State the blood parasite species.
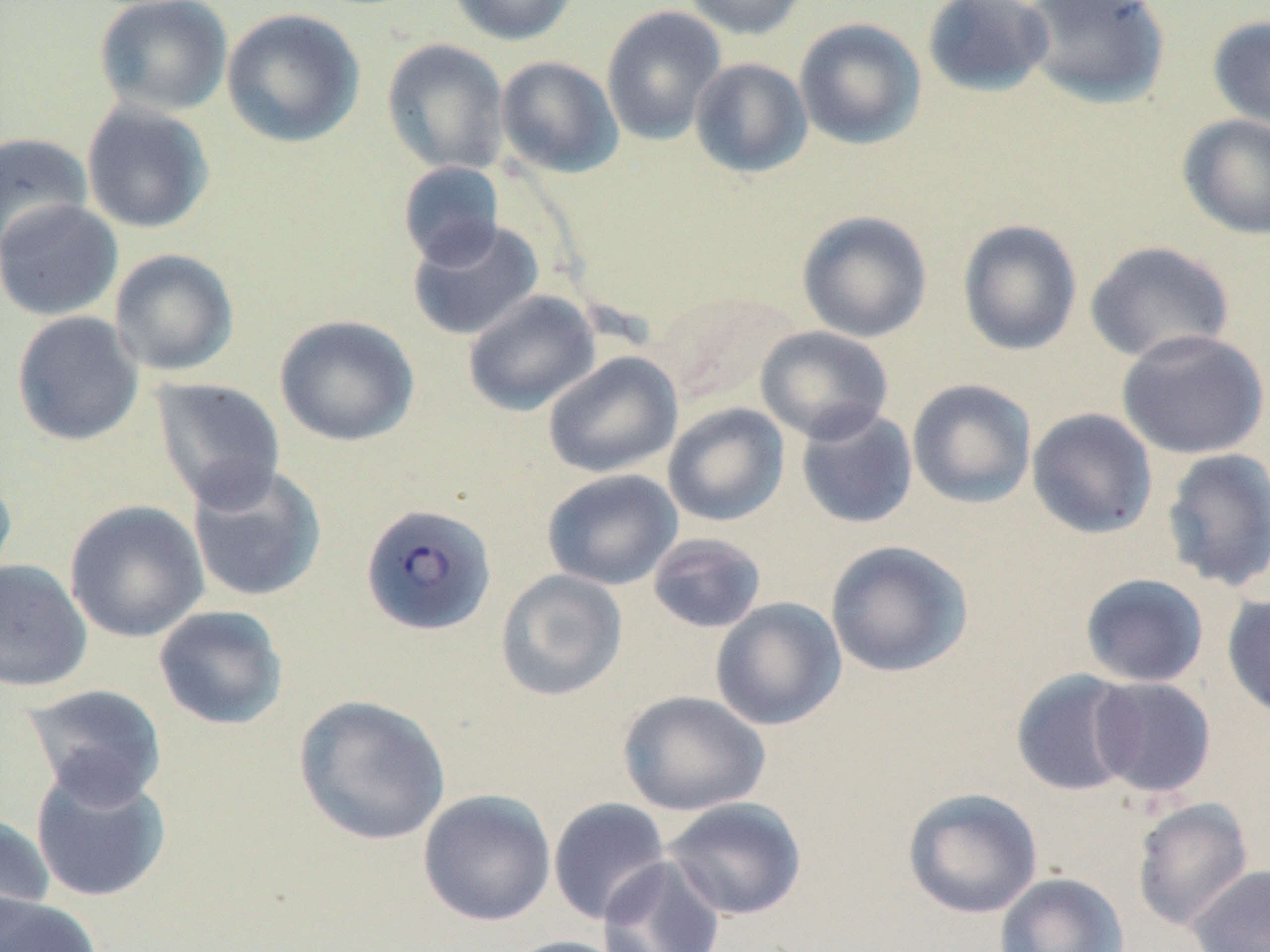
Plasmodium falciparum.

preparation = thin blood smear
magnification = 1000x
field of view = single
modality = optical microscopy
stain = May-Grünwald-Giemsa
Plasmodium falciparum-infected red blood cell locations = approximate bounding boxes as [x1, y1, x2, y2] in pixels: [359, 503, 497, 636]
image size = 1270×952 pixels
uninfected red blood cell locations = approximate bounding boxes as [x1, y1, x2, y2] in pixels: [447, 0, 579, 46], [680, 0, 810, 40], [922, 0, 1054, 97], [1022, 0, 1171, 110], [94, 1, 234, 117], [601, 6, 727, 146], [221, 8, 365, 148], [1207, 15, 1270, 133], [794, 18, 927, 150], [382, 39, 510, 175], [495, 55, 623, 178], [689, 57, 813, 178], [81, 101, 215, 234], [1177, 114, 1270, 240], [0, 132, 93, 255], [397, 161, 505, 269], [0, 199, 123, 321], [796, 210, 932, 343], [406, 218, 544, 342], [957, 219, 1083, 357], [1084, 241, 1236, 364], [109, 249, 239, 377], [462, 289, 601, 416], [659, 290, 800, 405], [11, 311, 144, 446], [274, 314, 420, 447], [755, 325, 894, 444], [1116, 329, 1269, 460], [542, 351, 683, 478], [149, 377, 287, 511], [907, 379, 1038, 509], [662, 403, 791, 526], [795, 406, 919, 530], [1026, 408, 1158, 539], [1161, 448, 1270, 593], [186, 463, 328, 604], [0, 468, 17, 594], [541, 469, 683, 590], [64, 500, 209, 643], [647, 532, 768, 634], [824, 539, 973, 678], [0, 559, 93, 693], [495, 569, 629, 702], [1079, 573, 1210, 687], [1222, 592, 1270, 721], [710, 597, 847, 731], [153, 605, 288, 730], [1010, 669, 1139, 796], [1089, 677, 1216, 799], [22, 684, 168, 808], [617, 690, 771, 816], [294, 694, 451, 846], [29, 763, 172, 904], [902, 787, 1043, 919], [417, 788, 557, 927], [663, 797, 808, 921], [1131, 797, 1253, 931], [547, 798, 672, 925], [0, 812, 56, 939], [596, 856, 727, 952], [1186, 864, 1270, 952], [994, 872, 1129, 952], [0, 893, 103, 952], [499, 935, 633, 952]